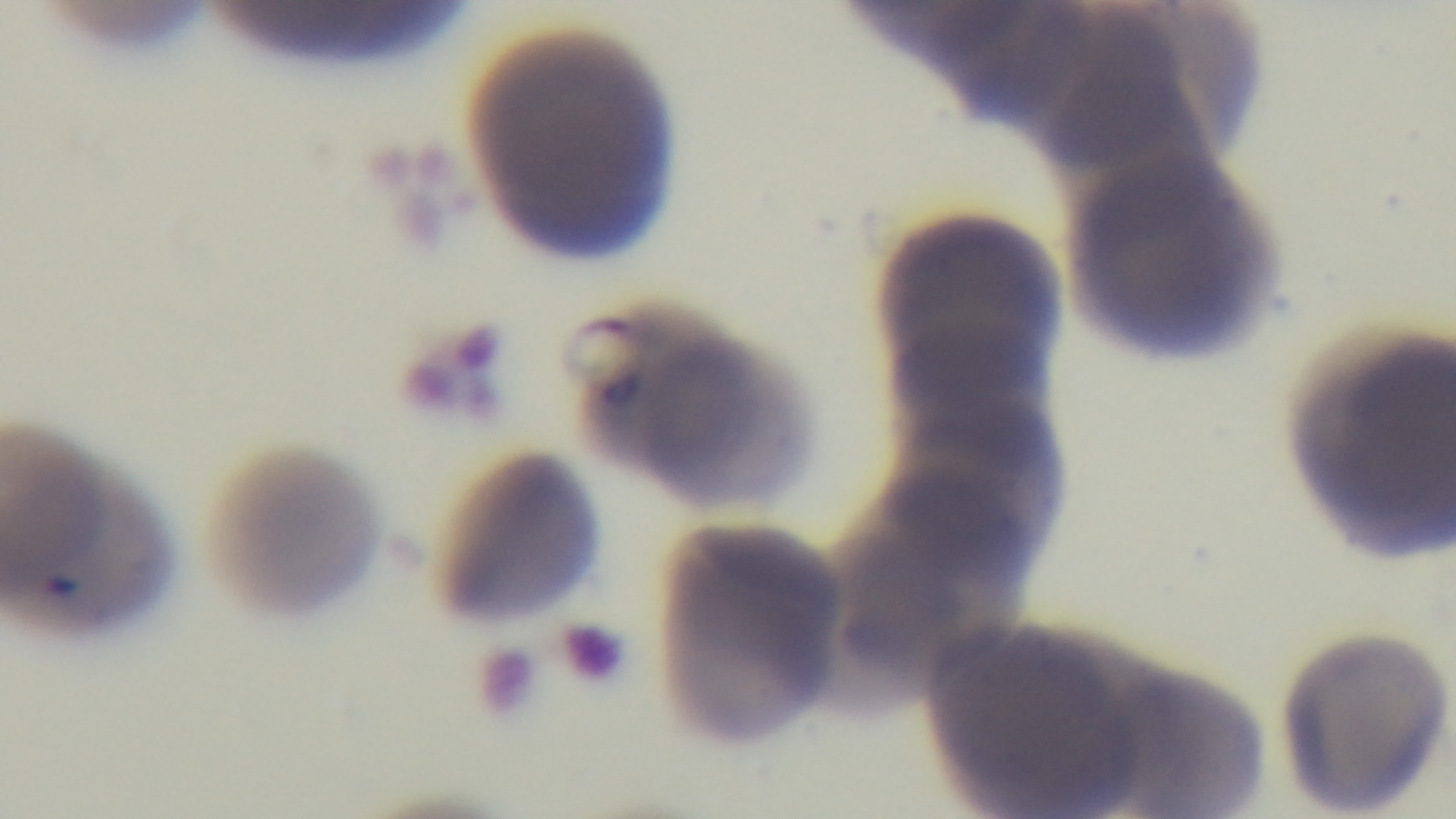
Summary:
  - Preparation: thin
  - Objective: 100x oil immersion
  - Capture: mounted 4K digital camera
  - Stain: Giemsa
  - Modality: light microscopy
  - Field of view: one from the slide
  - Malaria status: infected